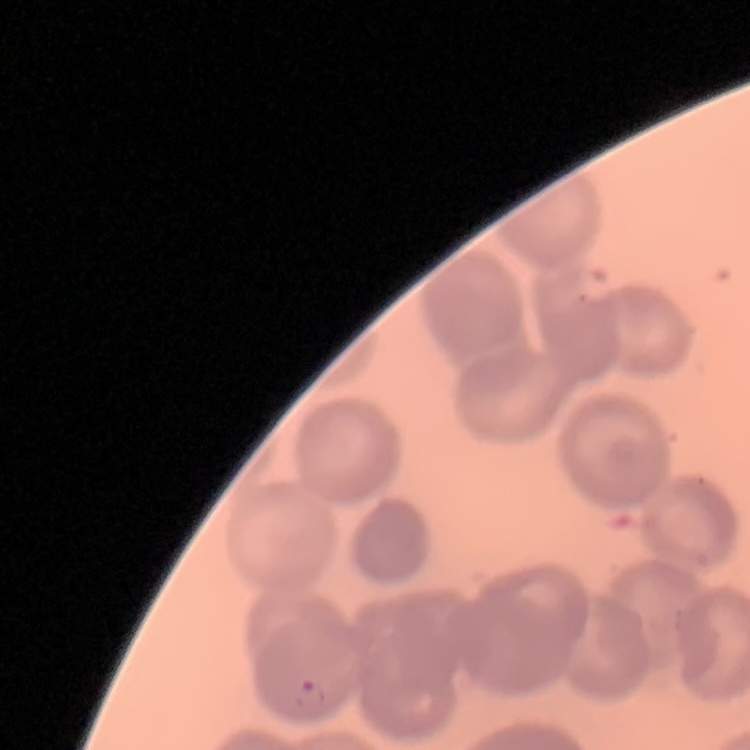
The erythrocytes exhibit no rouleaux formation. Field's or Giemsa stain. One tile cut from a larger photomicrograph. Thin blood smear.